Identify the parasite.
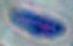
Toxoplasma gondii.

modality = photomicrograph
magnification = 1000x